Point out each leukocyte.
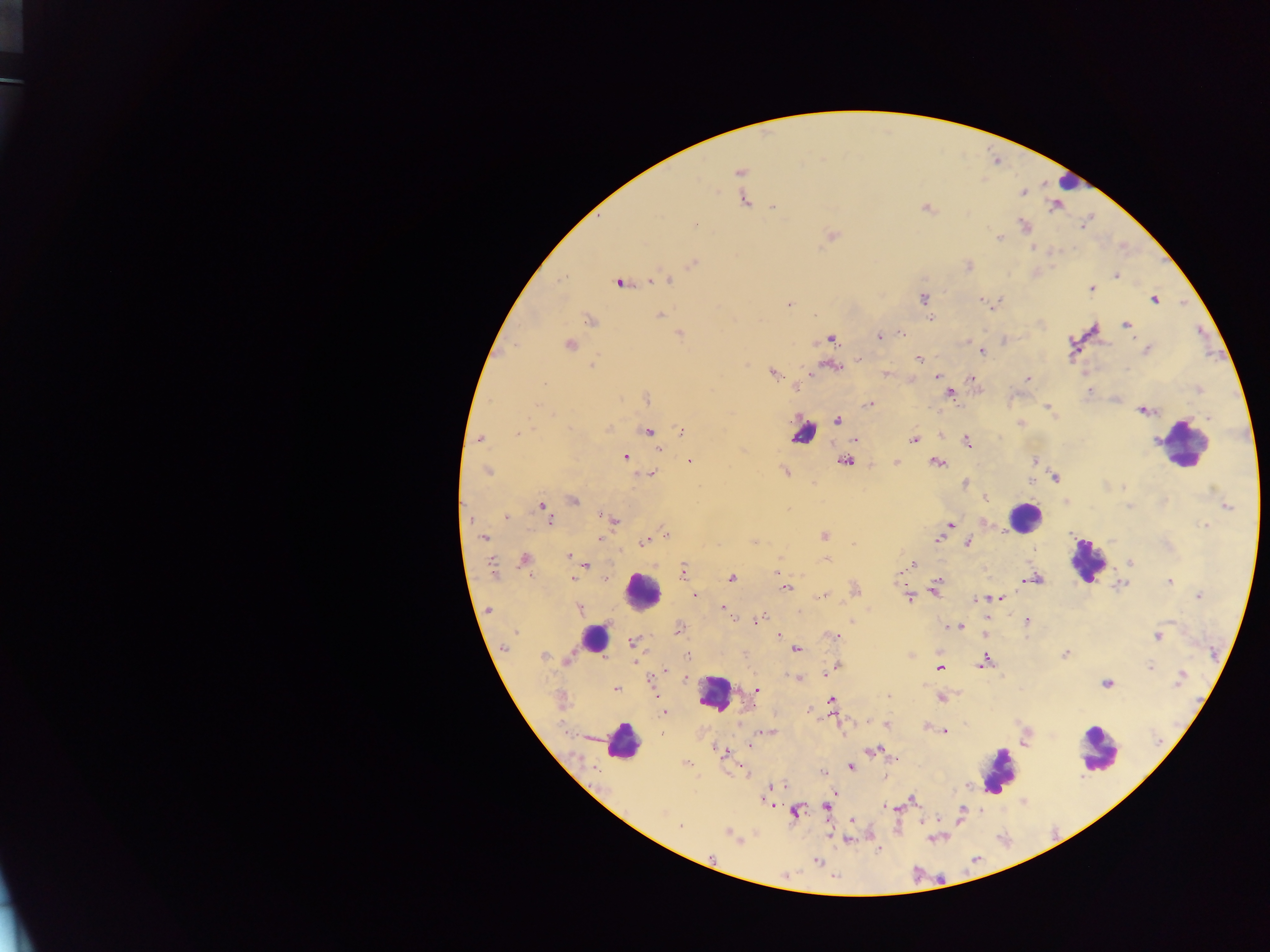

Approximate centers as {x, y} in pixels.
Leukocytes: {807, 429}, {1190, 447}, {1027, 516}, {1090, 558}, {645, 593}, {595, 639}, {713, 697}, {1102, 745}, {623, 748}, {997, 775}.

Malaria parasite locations: {745, 198}, {774, 208}, {925, 209}, {694, 225}, {831, 234}, {998, 237}, {694, 262}, {1115, 275}, {650, 281}, {671, 281}, {619, 282}, {1090, 290}, {1153, 298}, {923, 299}, {979, 299}, {788, 305}, {661, 313}, {589, 321}, {1126, 323}, {1095, 329}, {679, 334}, {879, 336}, {832, 339}, {1069, 341}, {570, 344}, {1146, 350}, {980, 352}, {918, 359}, {592, 364}, {772, 373}, {885, 375}, {936, 376}, {1026, 378}, {971, 379}, {543, 385}, {1088, 392}, {646, 398}, {869, 404}, {1046, 407}, {1141, 410}, {1049, 411}, {1052, 412}, {1208, 416}, {836, 419}, {1020, 422}, {607, 427}, {681, 431}, {518, 432}, {648, 432}, {479, 439}, {913, 439}, {854, 441}, {1156, 441}, {660, 449}, {625, 455}, {846, 460}, {689, 461}, {1035, 461}, {896, 462}, {936, 462}, {486, 471}, {786, 471}, {653, 472}, {1056, 478}, {1030, 481}, {965, 483}, {1124, 485}, {985, 498}, {574, 502}, {1066, 503}, {544, 504}, {1228, 506}, {506, 517}, {600, 517}, {615, 520}, {985, 521}, {949, 526}, {1203, 527}, {824, 535}, {484, 537}, {599, 538}, {936, 540}, {642, 542}, {753, 542}, {968, 542}, {567, 556}, {826, 559}, {525, 560}, {1130, 562}, {913, 563}, {586, 566}, {493, 567}, {684, 569}, {732, 577}, {574, 579}, {1036, 579}, {1167, 581}, {1022, 583}, {1119, 585}, {785, 588}, {933, 591}, {695, 595}, {820, 596}, {826, 596}, {1197, 596}, {908, 598}, {981, 600}, {1005, 600}, {721, 606}, {579, 609}, {488, 610}, {761, 617}, {757, 619}, {851, 622}, {1027, 622}, {960, 625}, {778, 633}, {833, 637}, {1158, 638}, {632, 643}, {500, 647}, {796, 648}, {503, 649}, {910, 654}, {545, 655}, {686, 655}, {1064, 656}, {568, 661}, {984, 661}, {979, 665}, {1150, 667}, {940, 670}, {1181, 671}, {826, 675}, {796, 679}, {1179, 682}, {1106, 684}, {615, 688}, {757, 688}, {887, 696}, {941, 698}, {830, 700}, {664, 710}, {886, 724}, {925, 726}, {944, 731}, {748, 745}, {718, 749}, {873, 749}, {685, 763}, {851, 767}, {745, 773}, {911, 798}, {773, 804}, {827, 806}, {796, 812}, {678, 827}, {729, 834}. Photographed through a microscope with a mobile-phone camera. One field of view. Image is 1270×952 pixels. Thick blood smear. Collected in Ghana.